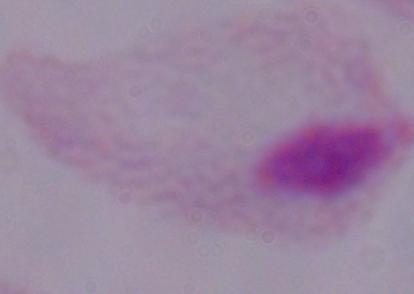

Summary:
  - Magnification: 1000x
  - Identification: trichomonad
  - Modality: photomicrograph